Point out each Plasmodium parasite and each leukocyte.
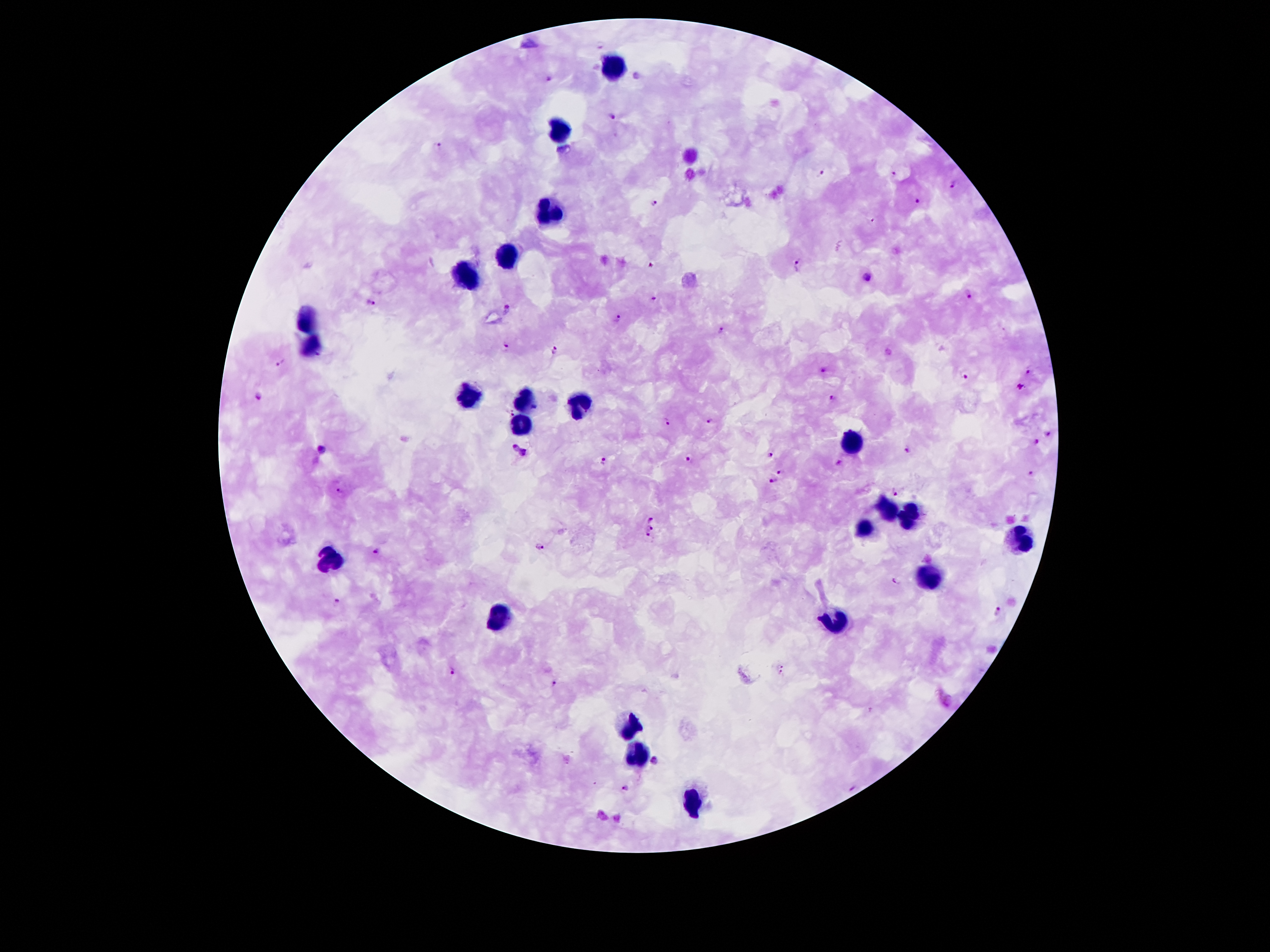
Approximate centers as {x, y} in pixels.
Plasmodium parasites: {548, 79}, {614, 118}, {440, 144}, {823, 174}, {895, 174}, {953, 184}, {918, 198}, {654, 203}, {651, 264}, {797, 265}, {869, 276}, {970, 295}, {655, 297}, {371, 303}, {509, 308}, {617, 316}, {723, 328}, {504, 346}, {555, 349}, {283, 363}, {1031, 369}, {823, 372}, {965, 375}, {1020, 386}, {833, 396}, {255, 397}, {711, 420}, {668, 422}, {1049, 435}, {1034, 442}, {511, 447}, {321, 448}, {907, 449}, {523, 452}, {772, 455}, {688, 457}, {602, 459}, {839, 463}, {783, 471}, {1032, 475}, {774, 481}, {342, 489}, {896, 491}, {651, 517}, {650, 528}, {648, 534}, {541, 547}, {375, 550}, {894, 581}, {336, 600}, {998, 611}, {781, 669}, {453, 670}, {554, 682}, {654, 761}, {625, 787}, {853, 788}.
Leukocytes: {614, 67}, {561, 130}, {549, 213}, {507, 258}, {465, 279}, {305, 316}, {309, 348}, {462, 398}, {525, 403}, {578, 408}, {523, 423}, {851, 444}, {888, 507}, {910, 514}, {865, 526}, {1021, 541}, {336, 557}, {930, 579}, {500, 615}, {836, 621}, {635, 722}, {635, 753}, {691, 799}.

Summary:
  - Stain: Giemsa
  - Capture: smartphone through the microscope eyepiece
  - Image size: 1270×952 pixels
  - Field of view: one from this slide
  - Preparation: thick peripheral-blood smear
  - Magnification: 100x
  - Patient malaria status: infected with Plasmodium falciparum